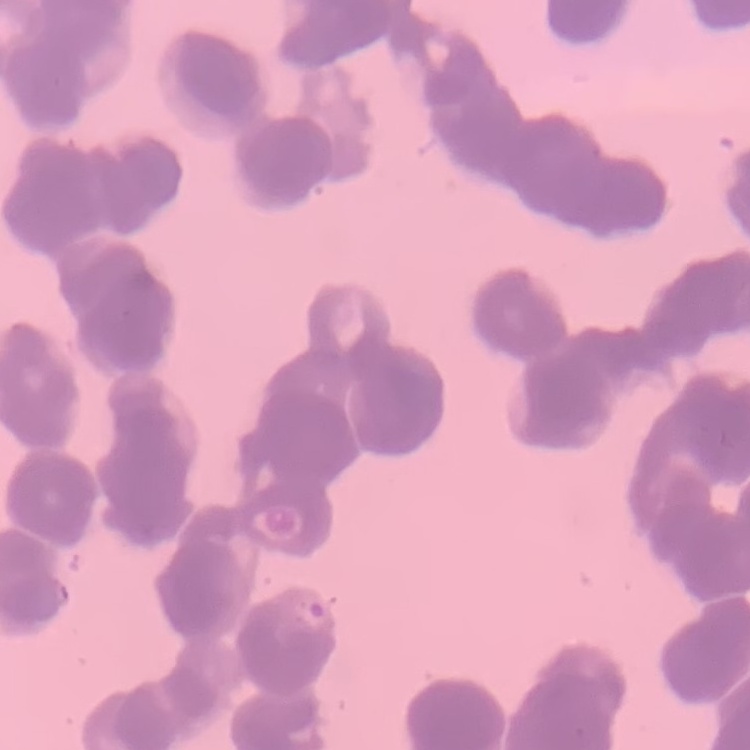 The red blood cells show rouleaux formation. Field's or Giemsa stain. Square crop of a larger photomicrograph. Thin blood smear.